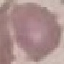
result = no malaria parasites detected
image type = automatically extracted cell patch, resized to 64 × 64 pixels
capture = smartphone camera at the microscope eyepiece
preparation = thin blood film
stain = Giemsa